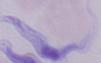

Summary:
  - Magnification: 1000x
  - Modality: micrograph
  - Identification: trypanosome